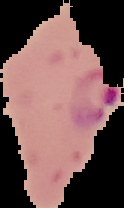

image size = 124×208 pixels
image type = segmented cell region on a black background
preparation = thin blood smear
result = malaria parasites identified